Report the malaria status of this cell.
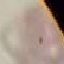

Uninfected.

Summary:
  - Stain: Giemsa
  - Image type: automatically extracted cell patch, resized to 64 × 64 pixels
  - Preparation: thin blood film
  - Capture: smartphone through the microscope eyepiece